Comment on the morphology of the erythrocytes.
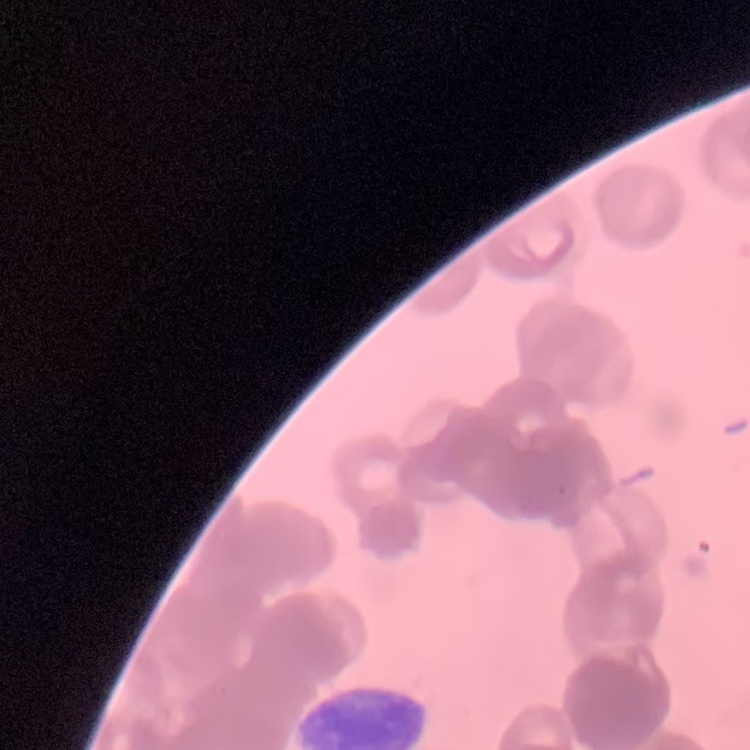
They show rouleaux formation.

{
  "preparation": "thin blood smear",
  "stain": "Field's or Giemsa",
  "image_type": "square crop of a larger photomicrograph"
}